Evaluate for Plasmodium parasites.
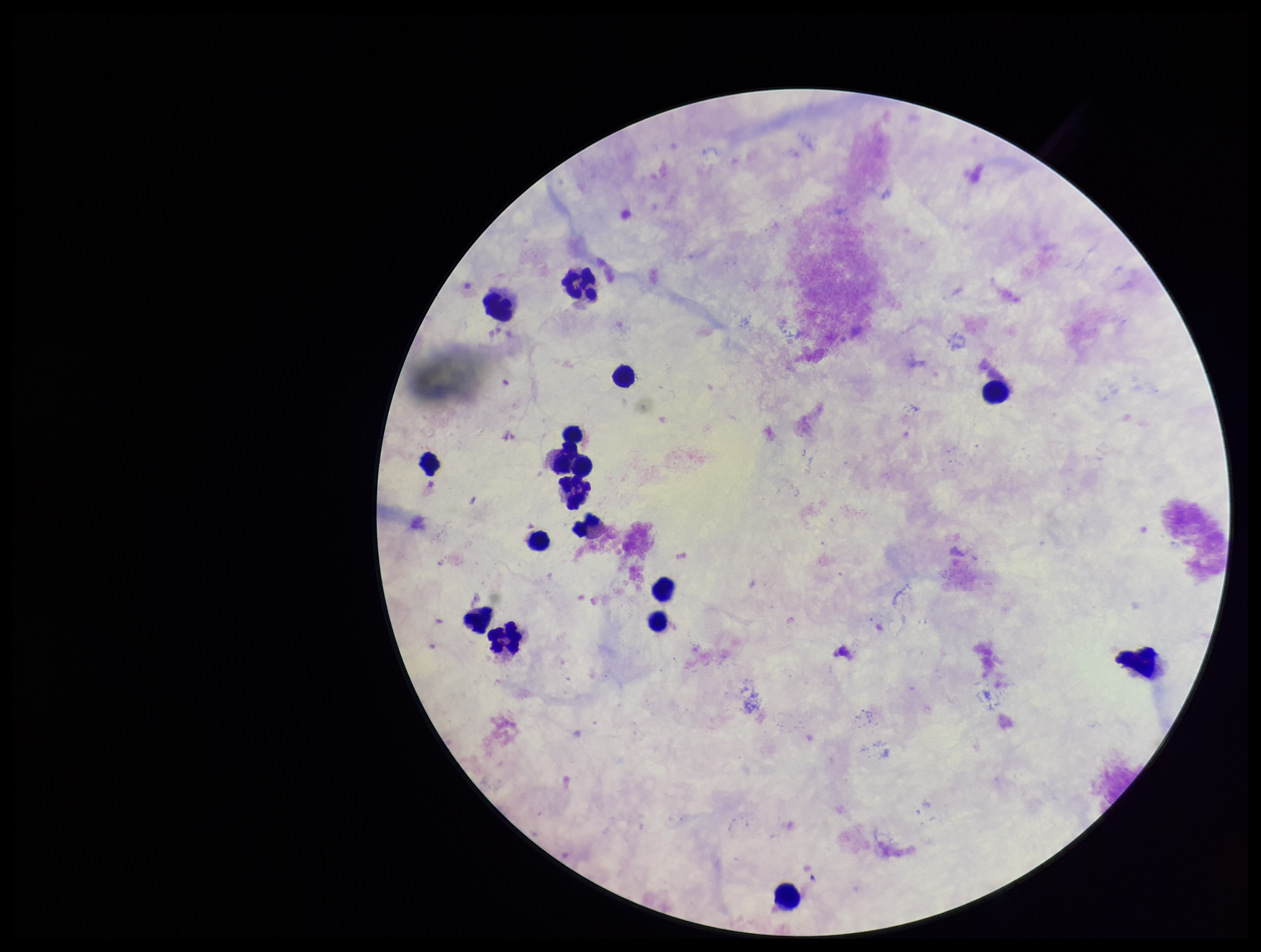
None detected.

preparation = thick blood smear
patient malaria status = negative
image size = 1261×952 pixels
field of view = one from this slide
parasite count = 0
leukocyte count = 16
stain = Giemsa
capture = smartphone photograph through the microscope eyepiece